Give the position of every Plasmodium parasite visible.
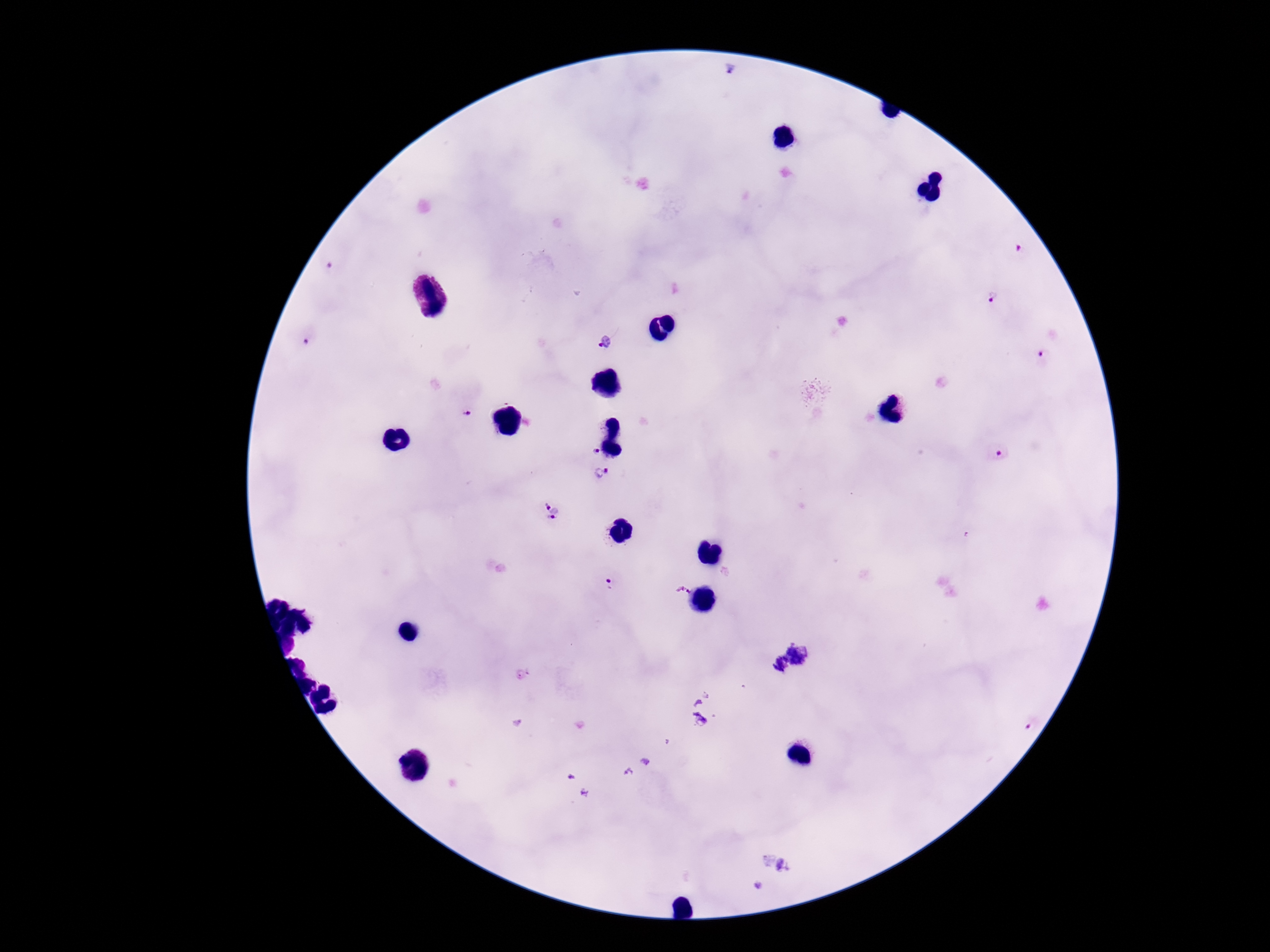
Approximate centers as [x, y] in pixels.
Plasmodium parasites: [732, 71], [329, 268], [991, 297], [306, 341], [603, 343], [1045, 356], [466, 415], [592, 452], [1000, 454], [601, 474], [552, 511], [611, 584], [683, 591].

Giemsa-stained preparation. Thick blood smear. Image is 1270×952 pixels. Single field of view. Patient malaria status: positive. 100x magnification. Smartphone photograph taken through the microscope eyepiece.